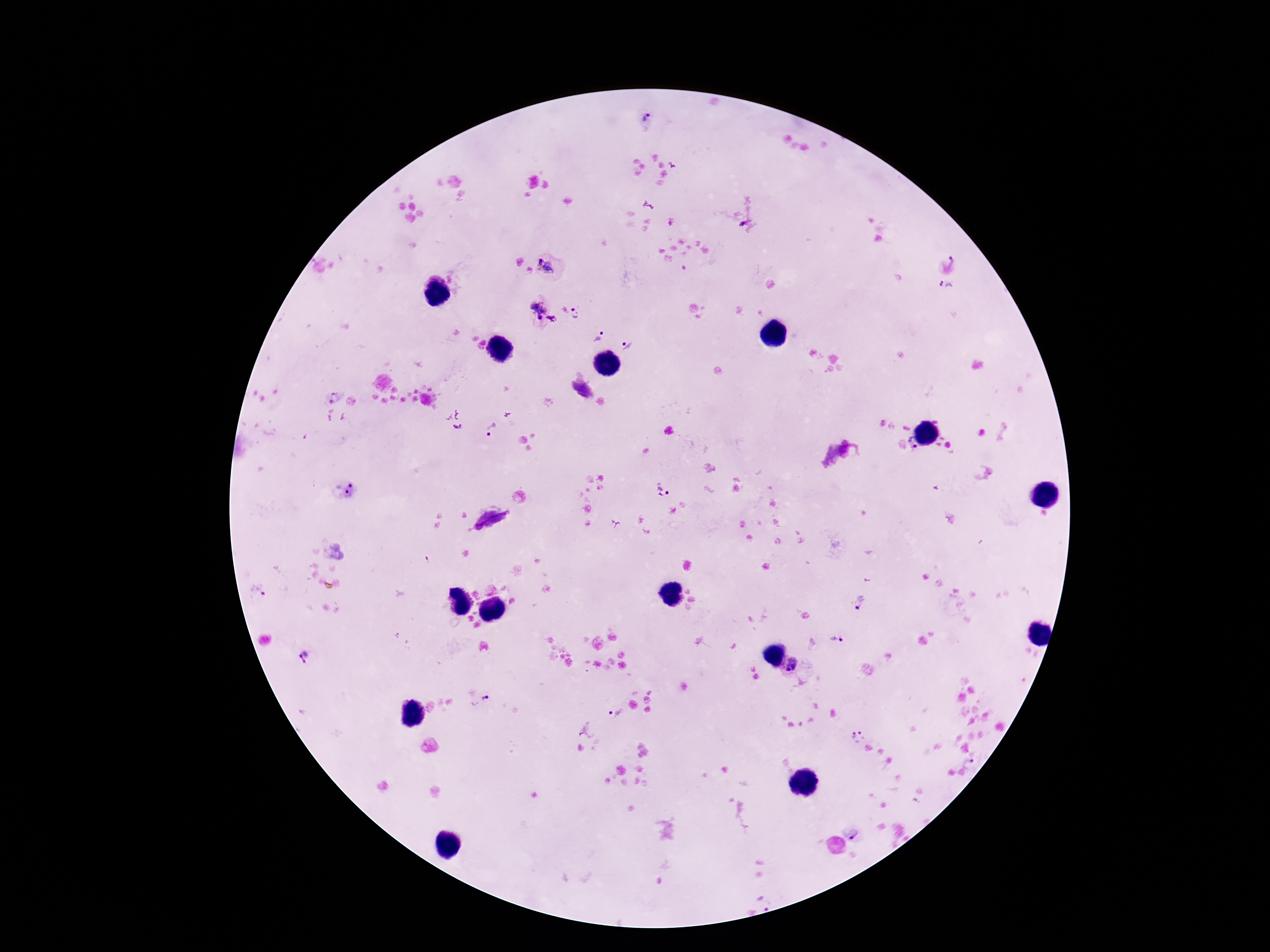 Approximate centers as {x, y} in pixels. Plasmodium parasite locations: {645, 116}, {743, 224}, {954, 261}, {548, 269}, {947, 288}, {537, 309}, {579, 313}, {552, 319}, {598, 336}, {629, 345}, {334, 397}, {491, 431}, {913, 445}, {342, 488}, {665, 491}, {492, 518}, {259, 592}, {860, 604}, {837, 638}, {304, 656}, {791, 666}, {478, 698}, {616, 710}, {863, 734}, {853, 739}, {971, 761}, {852, 834}, {765, 903}. Giemsa stain. One field from this slide. Image is 1270×952 pixels. Thick blood smear. Patient malaria status: positive. Photographed through the microscope eyepiece with a smartphone camera. 100x magnification.